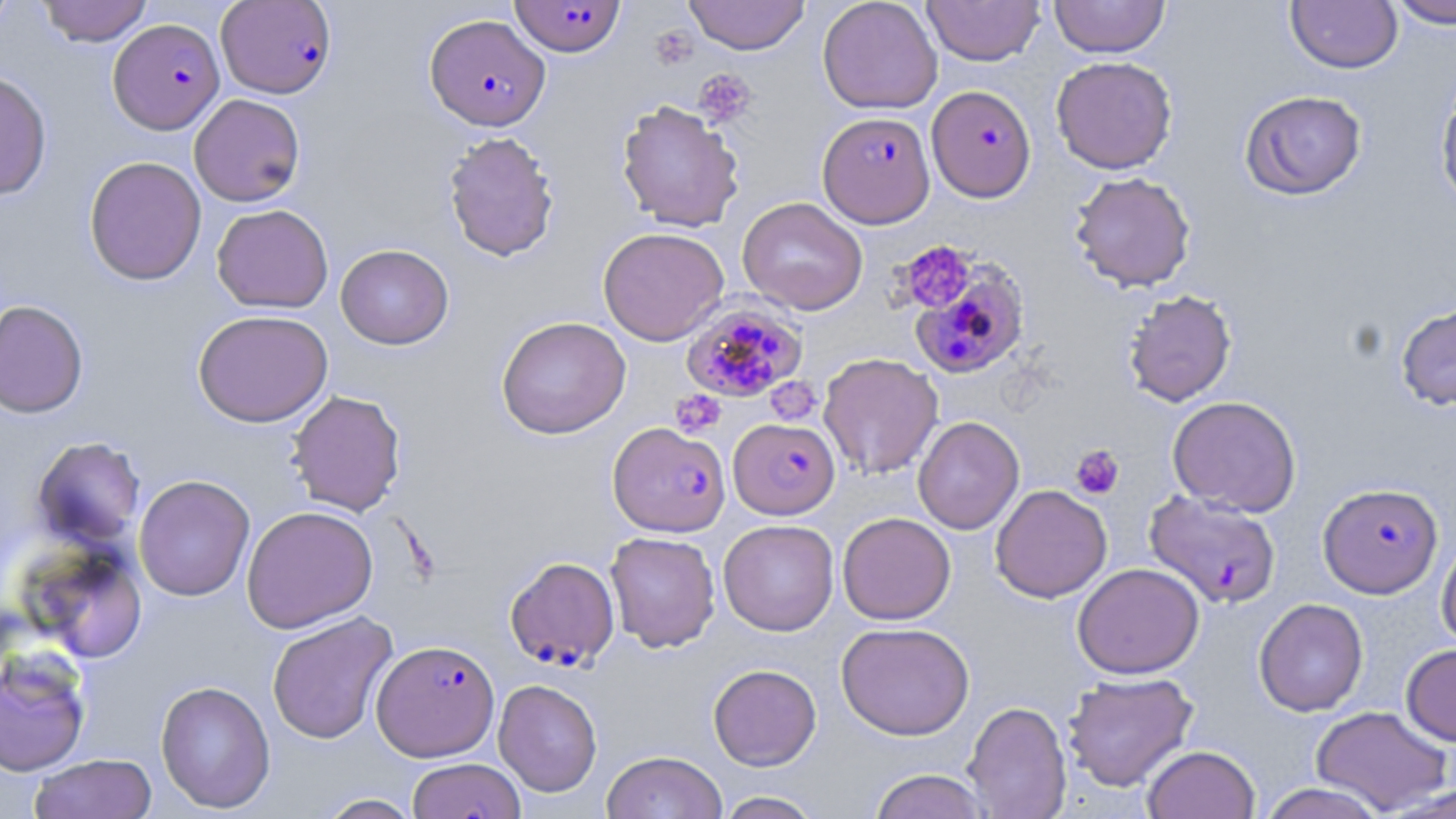 Approximate bounding boxes as named x1/y1/x2/y2 corners in pixels. Platelet locations: (x1=694, y1=69, x2=757, y2=126), (x1=898, y1=240, x2=977, y2=313), (x1=766, y1=377, x2=822, y2=424), (x1=670, y1=389, x2=726, y2=438), (x1=1070, y1=445, x2=1124, y2=499). Uninfected red blood cell locations (subset): (x1=0, y1=0, x2=19, y2=40), (x1=36, y1=0, x2=153, y2=46), (x1=683, y1=0, x2=810, y2=55), (x1=817, y1=0, x2=943, y2=114), (x1=922, y1=0, x2=1045, y2=65), (x1=1049, y1=0, x2=1170, y2=57), (x1=1386, y1=0, x2=1456, y2=29), (x1=1286, y1=1, x2=1403, y2=73), (x1=1051, y1=56, x2=1178, y2=174), (x1=0, y1=69, x2=52, y2=200), (x1=1434, y1=76, x2=1456, y2=213), (x1=1239, y1=90, x2=1367, y2=201), (x1=189, y1=94, x2=306, y2=207), (x1=616, y1=100, x2=745, y2=233), (x1=442, y1=130, x2=560, y2=262), (x1=84, y1=156, x2=206, y2=285), (x1=1069, y1=171, x2=1196, y2=292), (x1=737, y1=196, x2=868, y2=315), (x1=211, y1=204, x2=334, y2=313), (x1=598, y1=227, x2=729, y2=345), (x1=335, y1=244, x2=454, y2=349), (x1=1122, y1=289, x2=1237, y2=407), (x1=0, y1=299, x2=88, y2=419), (x1=1395, y1=302, x2=1456, y2=411), (x1=193, y1=309, x2=332, y2=427), (x1=496, y1=316, x2=631, y2=439), (x1=818, y1=352, x2=943, y2=479), (x1=285, y1=389, x2=407, y2=516), (x1=1167, y1=396, x2=1302, y2=516), (x1=912, y1=416, x2=1024, y2=534), (x1=31, y1=437, x2=146, y2=549), (x1=134, y1=474, x2=255, y2=601), (x1=990, y1=484, x2=1111, y2=603), (x1=241, y1=505, x2=378, y2=633), (x1=837, y1=512, x2=956, y2=625), (x1=718, y1=519, x2=838, y2=636), (x1=605, y1=531, x2=720, y2=652), (x1=1437, y1=534, x2=1456, y2=653), (x1=27, y1=543, x2=148, y2=663), (x1=1072, y1=562, x2=1204, y2=679), (x1=1254, y1=598, x2=1368, y2=716), (x1=266, y1=612, x2=398, y2=744), (x1=836, y1=621, x2=975, y2=740), (x1=1401, y1=643, x2=1456, y2=746), (x1=0, y1=650, x2=92, y2=776), (x1=708, y1=664, x2=822, y2=770), (x1=1061, y1=672, x2=1199, y2=792), (x1=493, y1=679, x2=602, y2=796), (x1=155, y1=680, x2=275, y2=813), (x1=962, y1=700, x2=1072, y2=819), (x1=1311, y1=706, x2=1453, y2=815), (x1=1142, y1=744, x2=1260, y2=819), (x1=601, y1=750, x2=727, y2=819), (x1=29, y1=754, x2=157, y2=819), (x1=406, y1=757, x2=526, y2=819), (x1=868, y1=769, x2=991, y2=818), (x1=1257, y1=783, x2=1388, y2=819), (x1=714, y1=791, x2=825, y2=818), (x1=314, y1=793, x2=424, y2=818). Plasmodium falciparum-infected red blood cell locations (subset): (x1=509, y1=0, x2=627, y2=56), (x1=216, y1=1, x2=337, y2=98), (x1=425, y1=13, x2=551, y2=131), (x1=108, y1=19, x2=224, y2=134), (x1=926, y1=85, x2=1036, y2=202), (x1=909, y1=259, x2=1032, y2=381), (x1=681, y1=300, x2=807, y2=404), (x1=728, y1=418, x2=840, y2=519), (x1=607, y1=421, x2=730, y2=537), (x1=1318, y1=482, x2=1443, y2=598), (x1=1144, y1=490, x2=1282, y2=609), (x1=505, y1=556, x2=620, y2=671), (x1=372, y1=639, x2=499, y2=761). Slide-level diagnosis: Plasmodium falciparum. One field of a larger specimen. Captured at 1000x magnification. Thin blood smear. Light microscopy. May-Grünwald-Giemsa stain. Image is 1456×819 pixels.